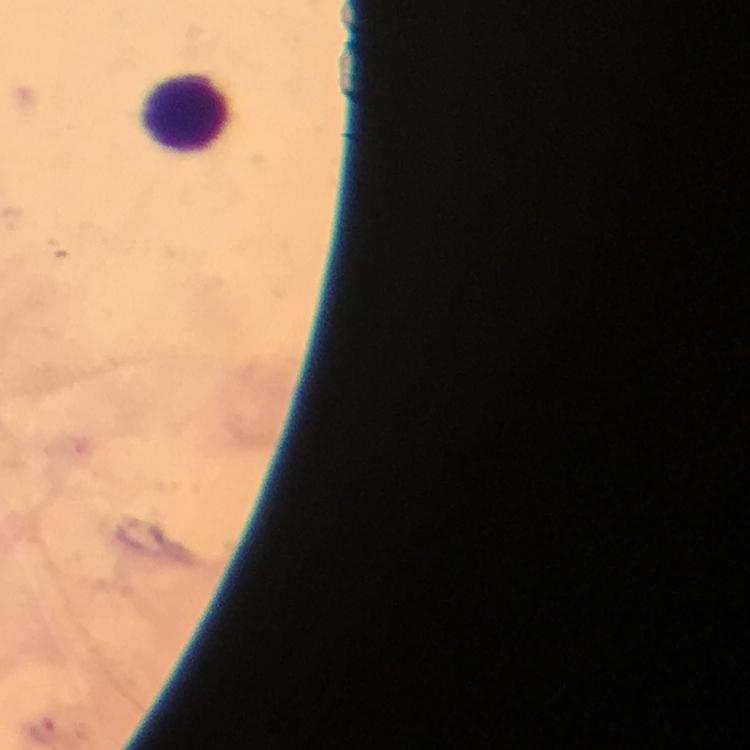

Approximate centers as [x, y] in pixels. Leukocyte locations: [187, 114]. Image is 750×750 pixels. Photographed through the microscope with a smartphone camera. Thick blood smear. From a malaria diagnostic workup. A crop from one field of view. 100x magnification. Giemsa-stained preparation. Malaria parasites: none seen. Immersion oil was used.